Evaluate for Plasmodium parasites.
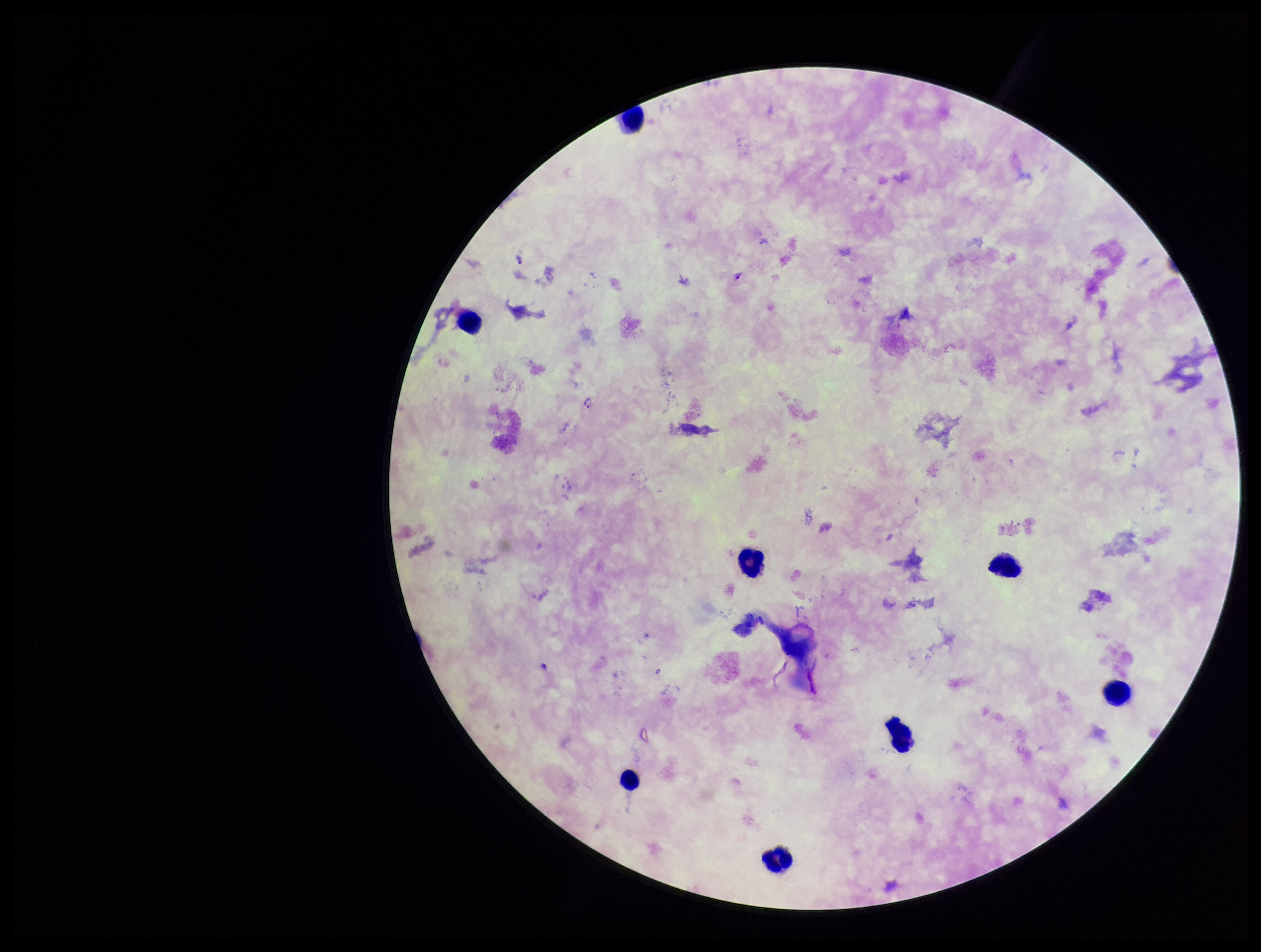
Detected.

{
  "leukocyte_count": 8,
  "field_of_view": "one from this slide",
  "image_size": "1261×952 pixels",
  "capture": "smartphone photograph through the microscope eyepiece",
  "species_reported_for_this_patient": "Plasmodium falciparum",
  "parasite_count": 3,
  "patient_malaria_status": "infected",
  "preparation": "thick smear",
  "stain": "Giemsa"
}